Locate every Plasmodium falciparum-infected red blood cell.
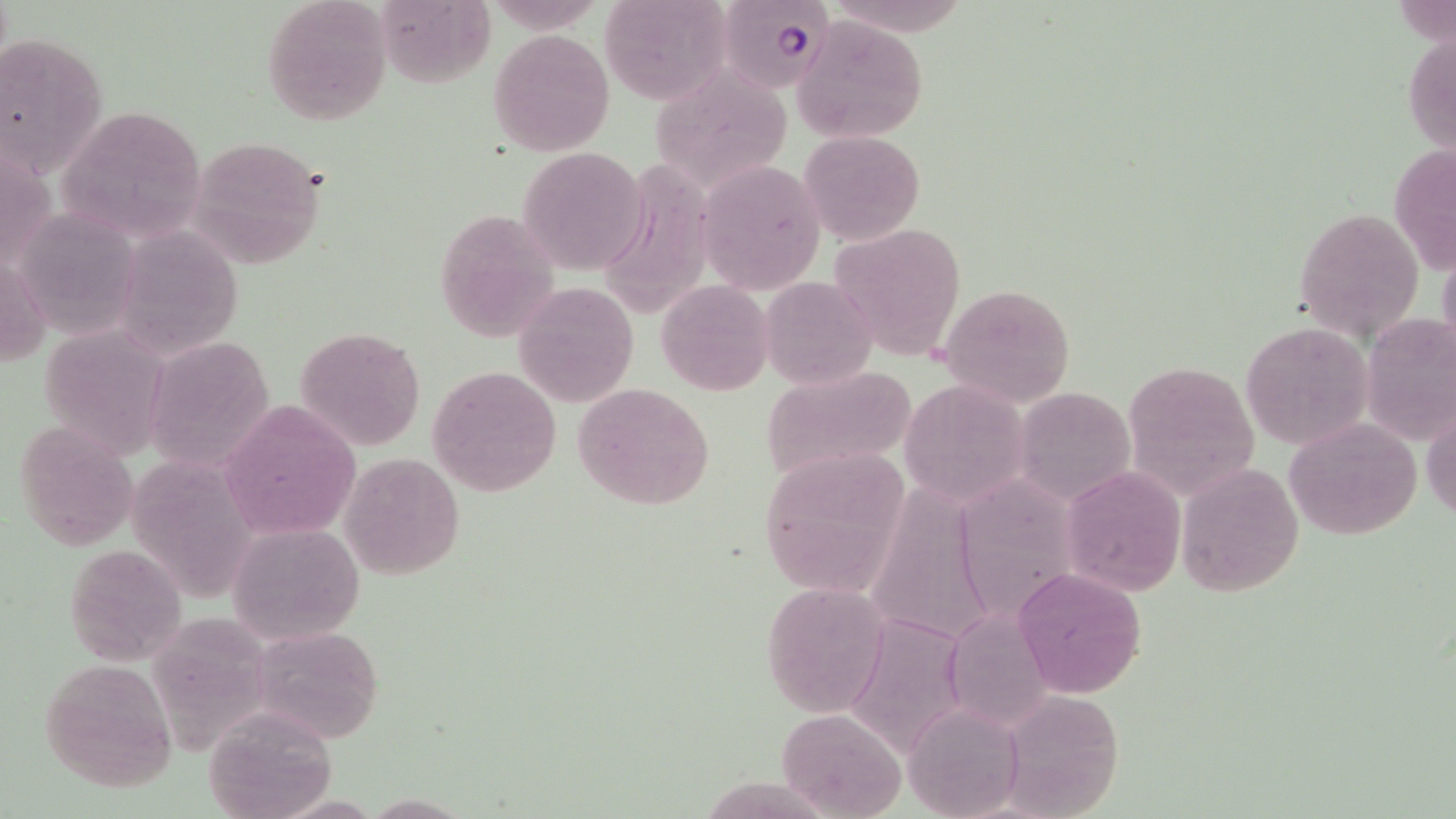
Approximate bounding boxes as [x1, y1, x2, y2] in pixels.
Plasmodium falciparum-infected red blood cells: [721, 0, 838, 92].

Summary:
  - Uninfected red blood cell locations: [600, 0, 731, 104], [261, 1, 392, 126], [379, 9, 512, 90], [795, 17, 928, 143], [1404, 23, 1456, 167], [489, 27, 616, 155], [1, 28, 108, 187], [650, 61, 788, 186], [52, 104, 211, 245], [799, 129, 925, 246], [188, 134, 327, 268], [1388, 140, 1456, 277], [517, 145, 650, 273], [621, 154, 724, 315], [699, 161, 829, 293], [1293, 206, 1424, 343], [13, 207, 144, 341], [431, 209, 560, 339], [828, 222, 968, 360], [116, 223, 243, 357], [1437, 241, 1456, 372], [1, 253, 48, 369], [760, 274, 877, 390], [655, 281, 773, 395], [512, 283, 639, 406], [937, 283, 1076, 408], [1359, 314, 1456, 448], [1240, 320, 1373, 452], [293, 326, 427, 450], [54, 330, 168, 462], [143, 336, 274, 470], [1119, 360, 1259, 500], [428, 365, 563, 497], [758, 365, 919, 484], [899, 378, 1031, 506], [572, 381, 716, 511], [1012, 385, 1136, 505], [1422, 397, 1455, 525], [220, 400, 360, 543], [1286, 416, 1423, 540], [13, 417, 138, 551], [753, 447, 913, 604], [111, 453, 259, 603], [341, 454, 465, 579], [1177, 462, 1304, 598], [1061, 467, 1186, 594], [971, 468, 1083, 621], [877, 485, 1001, 643], [231, 524, 366, 644], [63, 541, 188, 668], [1012, 567, 1147, 699], [760, 579, 893, 717], [153, 610, 273, 752], [842, 610, 972, 760], [948, 613, 1055, 733], [249, 624, 385, 744], [39, 658, 180, 793], [999, 689, 1128, 818], [902, 702, 1024, 819], [201, 705, 338, 818], [777, 707, 907, 819], [360, 793, 475, 817]
  - Slide-level diagnosis: Plasmodium falciparum
  - Stain: May-Grünwald-Giemsa
  - Preparation: thin blood smear
  - Image size: 1456×819 pixels
  - Magnification: 1000x
  - Modality: optical microscopy
  - Field of view: single